Classify this cell by malaria status.
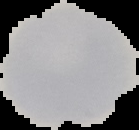
It is uninfected.

From a thin blood film. Image is 139×130 pixels. Cell region segmented out of the field of view; the surrounding area is masked to black.